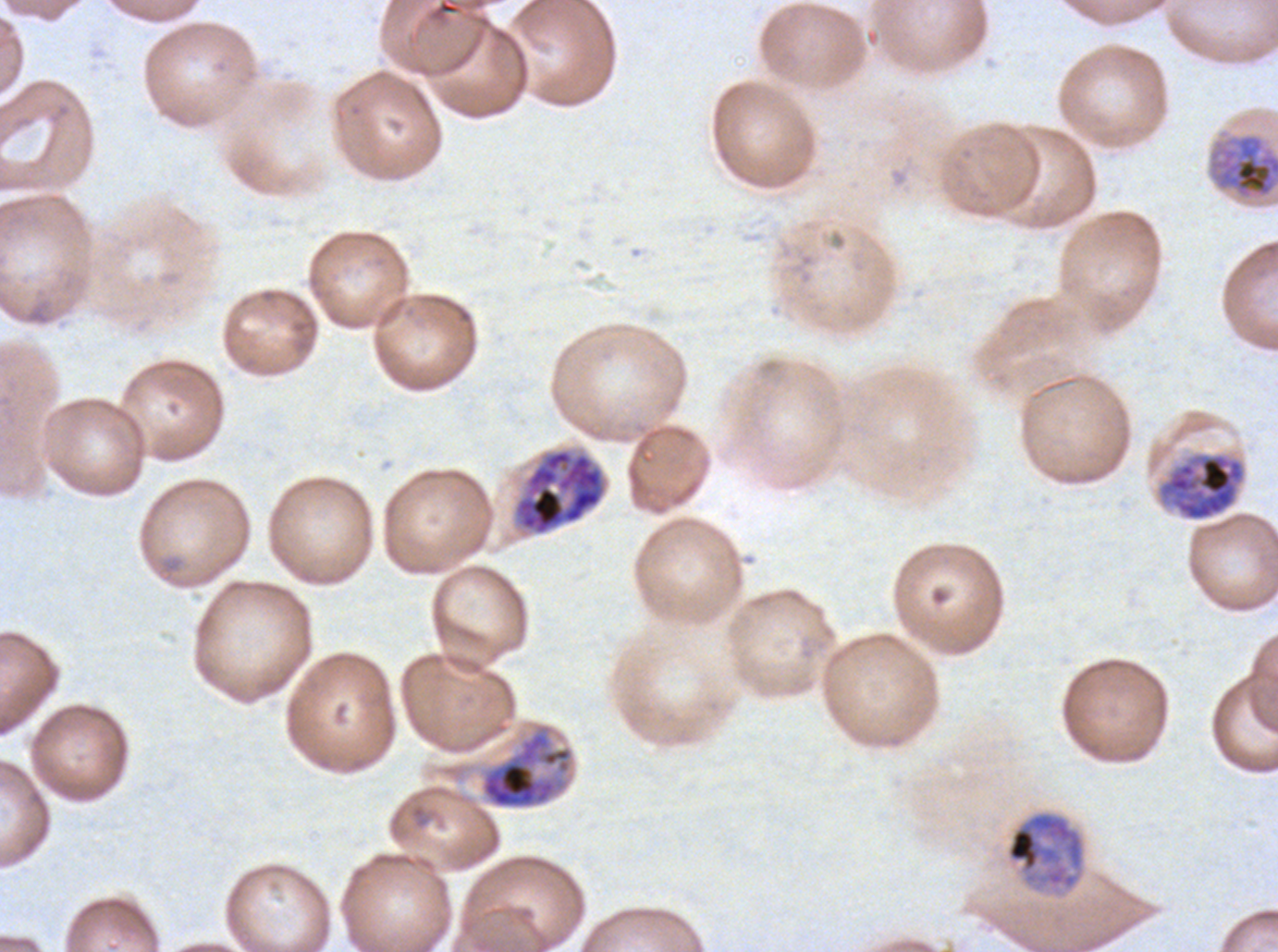
Approximate bounding boxes as {x1, y1, x2, y2} in pixels.
Summary:
  - Early schizont locations: {1206, 128, 1277, 202}, {513, 448, 606, 536}, {1157, 452, 1247, 521}, {479, 723, 574, 810}, {1004, 810, 1087, 897}
  - Image size: 1278×952 pixels
  - Field of view: sub-image separated from a larger composite
  - Stain: Giemsa
  - Specimen: P. falciparum from a patient in The Gambia, cultured ex vivo for 24 to 48 hours
  - Preparation: thin blood film